Identify the parasite.
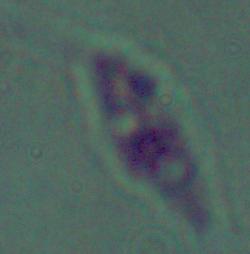
This is Leishmania.

Photomicrograph. Captured at 1000x magnification.